Locate every Trypanosoma brucei.
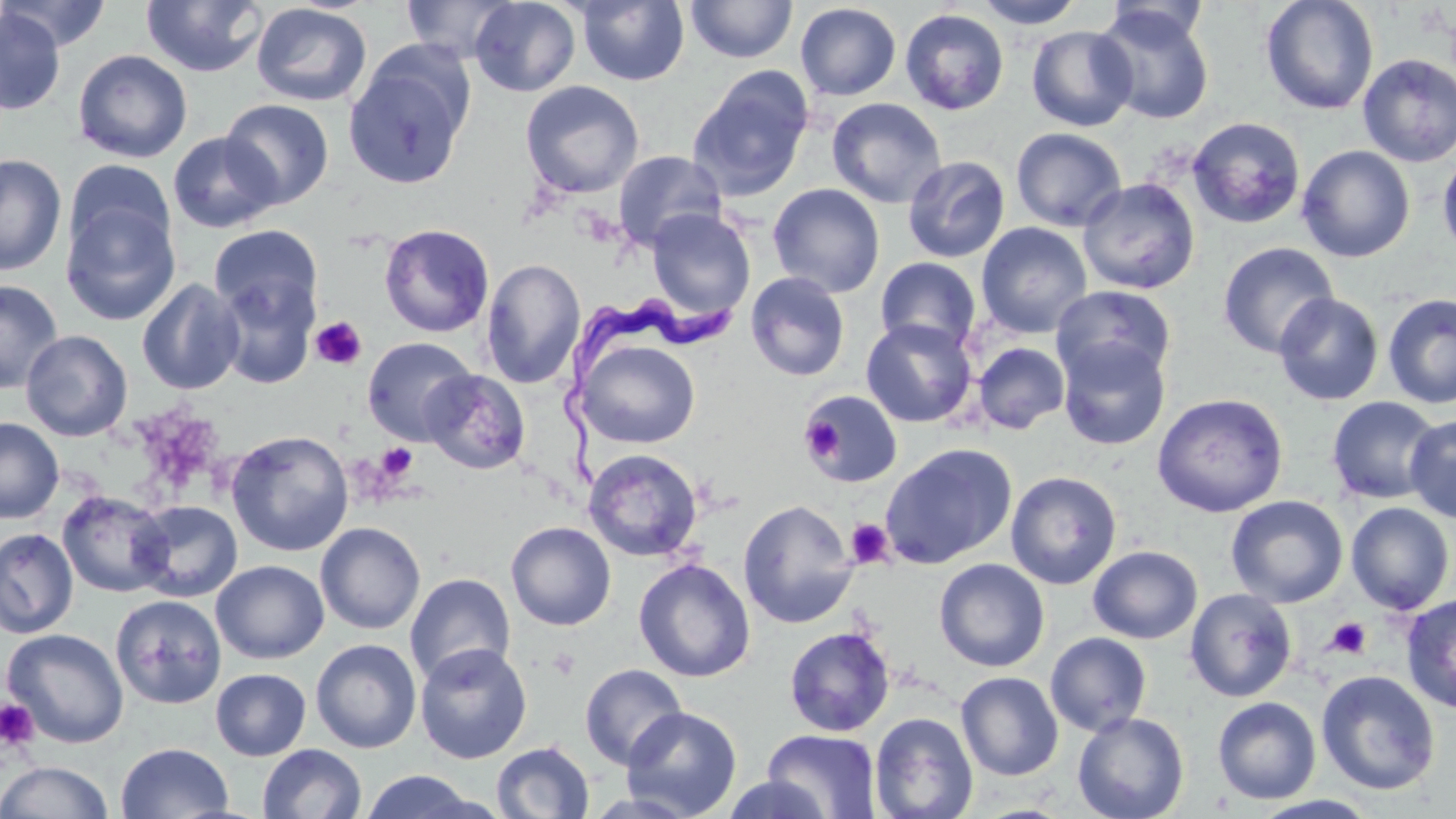
Approximate bounding boxes as (x1, y1, x2, y2) in pixels.
Trypanosoma brucei: (556, 290, 753, 491).

slide-level diagnosis = Trypanosoma brucei
modality = optical microscopy
magnification = 1000x
image size = 1456×819 pixels
stain = May-Grünwald-Giemsa
uninfected red blood cell locations = approximate bounding boxes as (x1, y1, x2, y2) in pixels: (1, 0, 113, 52), (400, 0, 521, 63), (469, 0, 581, 97), (574, 0, 690, 86), (686, 0, 798, 63), (972, 0, 1086, 29), (1259, 0, 1380, 115), (140, 1, 268, 77), (250, 2, 373, 107), (795, 3, 901, 101), (1094, 5, 1214, 124), (0, 8, 66, 116), (900, 9, 1009, 115), (1026, 25, 1138, 131), (343, 49, 474, 189), (73, 50, 193, 163), (1357, 53, 1456, 167), (688, 70, 813, 201), (520, 80, 644, 199), (827, 97, 947, 208), (220, 98, 334, 208), (1188, 116, 1305, 229), (1011, 127, 1127, 231), (167, 131, 282, 233), (1297, 144, 1416, 263), (612, 150, 727, 252), (1438, 151, 1456, 261), (0, 154, 67, 276), (902, 155, 1010, 263), (63, 160, 175, 260), (1078, 177, 1200, 294), (767, 183, 885, 298), (60, 203, 180, 326), (646, 208, 756, 319), (976, 222, 1092, 339), (379, 223, 494, 337), (209, 224, 323, 325), (1217, 242, 1339, 359), (874, 256, 982, 354), (480, 258, 585, 388), (745, 271, 850, 381), (214, 273, 319, 389), (136, 278, 245, 395), (0, 279, 64, 393), (1052, 285, 1176, 386), (1274, 292, 1384, 406), (1382, 294, 1456, 409), (861, 318, 978, 428), (20, 330, 133, 442), (361, 337, 478, 445), (1058, 337, 1171, 450), (578, 339, 700, 449), (972, 342, 1070, 434), (422, 369, 530, 474), (801, 388, 904, 490), (1151, 392, 1289, 517), (1326, 396, 1443, 505), (1404, 415, 1456, 523), (0, 417, 64, 524), (226, 430, 354, 556), (879, 442, 1017, 569), (583, 448, 703, 562), (1005, 471, 1122, 589), (57, 490, 173, 598), (1225, 495, 1348, 607), (738, 498, 859, 629), (132, 500, 243, 602), (1346, 502, 1455, 614), (506, 521, 616, 630), (315, 522, 426, 634), (0, 527, 79, 639), (1087, 545, 1202, 644), (634, 558, 756, 683), (934, 558, 1050, 672), (211, 560, 328, 664), (404, 572, 516, 686), (1185, 587, 1297, 702), (1400, 593, 1456, 713), (111, 594, 227, 709), (783, 625, 895, 737), (2, 628, 129, 747), (1045, 632, 1152, 736), (311, 638, 422, 753), (415, 642, 532, 763), (579, 663, 688, 769), (210, 668, 311, 760), (1316, 670, 1440, 796), (956, 671, 1063, 780), (1212, 696, 1322, 804), (621, 706, 742, 818), (869, 711, 978, 819), (1072, 711, 1190, 819), (762, 729, 882, 818), (491, 741, 595, 819), (116, 742, 233, 819), (258, 744, 367, 819), (0, 761, 114, 818), (358, 770, 490, 818), (717, 774, 835, 819)
platelet locations = approximate bounding boxes as (x1, y1, x2, y2) in pixels: (310, 316, 367, 370), (800, 417, 843, 461), (376, 443, 418, 481), (846, 519, 894, 568), (1326, 617, 1371, 659), (0, 699, 39, 751)
preparation = thin blood smear
field of view = single